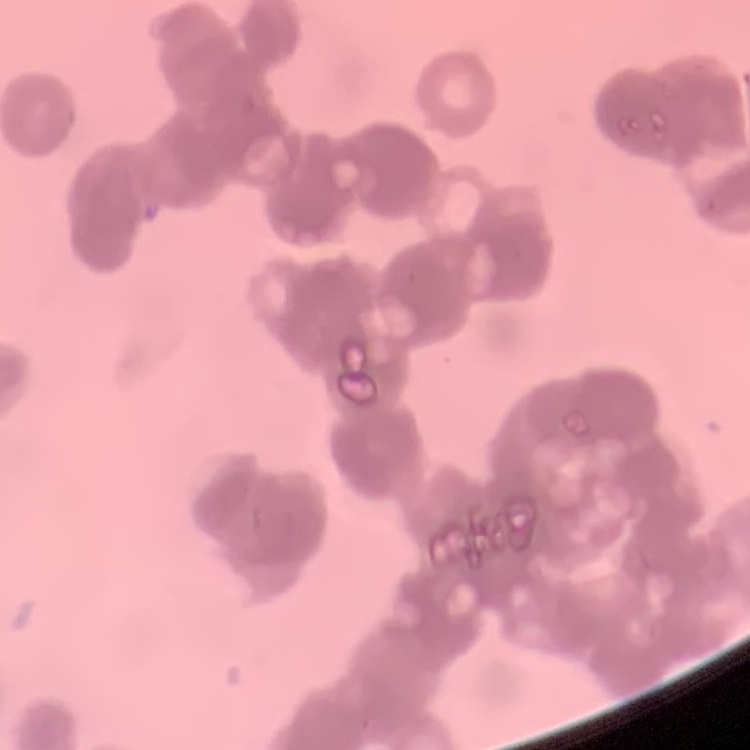

Summary:
  - Erythrocyte morphology: rouleaux formation
  - Stain: Field's or Giemsa
  - Preparation: thin peripheral smear
  - Image type: square crop of a larger photomicrograph